State the blood parasite species.
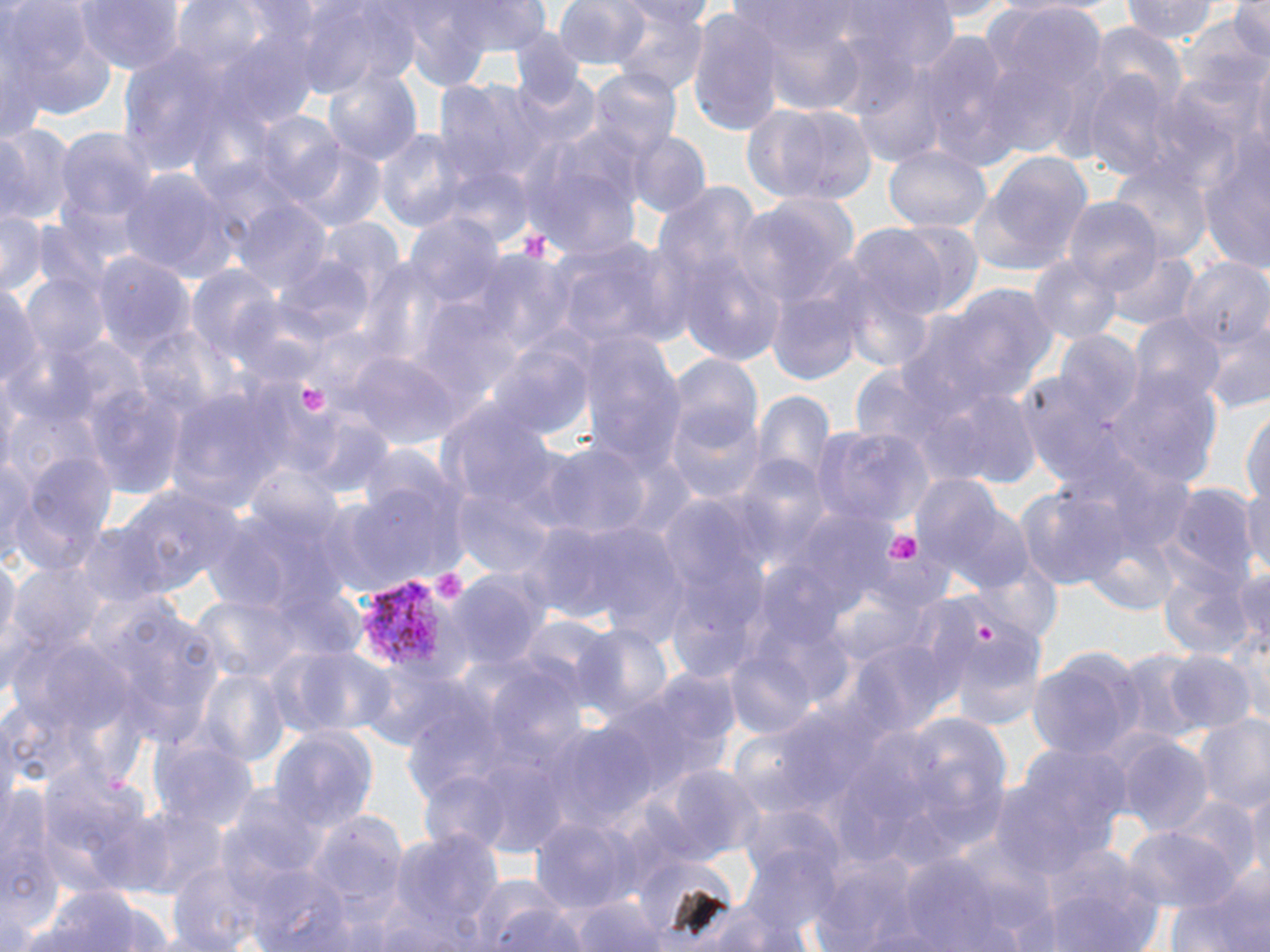
Plasmodium vivax.

Approximate bounding boxes as named x1/y1/x2/y2 corners in pixels. Uninfected red blood cell locations: (x1=74, y1=0, x2=185, y2=78), (x1=171, y1=0, x2=281, y2=83), (x1=295, y1=0, x2=422, y2=94), (x1=552, y1=0, x2=655, y2=69), (x1=1125, y1=0, x2=1222, y2=44), (x1=1230, y1=0, x2=1270, y2=64), (x1=439, y1=1, x2=553, y2=56), (x1=979, y1=1, x2=1106, y2=148), (x1=393, y1=2, x2=517, y2=85), (x1=4, y1=4, x2=119, y2=132), (x1=612, y1=7, x2=708, y2=98), (x1=687, y1=8, x2=785, y2=138), (x1=1086, y1=24, x2=1186, y2=113), (x1=909, y1=29, x2=1025, y2=167), (x1=107, y1=49, x2=230, y2=180), (x1=323, y1=66, x2=422, y2=169), (x1=589, y1=68, x2=680, y2=162), (x1=1080, y1=70, x2=1174, y2=178), (x1=434, y1=81, x2=550, y2=188), (x1=745, y1=101, x2=878, y2=204), (x1=249, y1=111, x2=347, y2=201), (x1=0, y1=123, x2=73, y2=230), (x1=55, y1=127, x2=155, y2=231), (x1=1198, y1=128, x2=1270, y2=274), (x1=626, y1=129, x2=710, y2=218), (x1=374, y1=130, x2=467, y2=235), (x1=520, y1=134, x2=643, y2=262), (x1=288, y1=140, x2=385, y2=232), (x1=881, y1=144, x2=993, y2=235), (x1=969, y1=153, x2=1093, y2=274), (x1=1109, y1=157, x2=1212, y2=266), (x1=441, y1=166, x2=533, y2=245), (x1=121, y1=172, x2=241, y2=285), (x1=652, y1=192, x2=792, y2=367), (x1=735, y1=196, x2=854, y2=312), (x1=1065, y1=199, x2=1164, y2=299), (x1=234, y1=200, x2=332, y2=294), (x1=1, y1=208, x2=44, y2=296), (x1=407, y1=214, x2=504, y2=311), (x1=883, y1=221, x2=983, y2=314), (x1=844, y1=227, x2=952, y2=330), (x1=554, y1=241, x2=672, y2=353), (x1=1106, y1=250, x2=1199, y2=334), (x1=89, y1=251, x2=195, y2=364), (x1=1030, y1=253, x2=1125, y2=346), (x1=279, y1=256, x2=373, y2=342), (x1=1183, y1=256, x2=1269, y2=352), (x1=185, y1=267, x2=281, y2=362), (x1=764, y1=272, x2=871, y2=387), (x1=0, y1=280, x2=44, y2=401), (x1=923, y1=282, x2=1060, y2=409), (x1=233, y1=299, x2=328, y2=389), (x1=1131, y1=313, x2=1226, y2=411), (x1=135, y1=325, x2=228, y2=422), (x1=1200, y1=325, x2=1270, y2=416), (x1=1054, y1=333, x2=1146, y2=424), (x1=580, y1=338, x2=687, y2=474), (x1=490, y1=341, x2=599, y2=444), (x1=348, y1=352, x2=464, y2=448), (x1=669, y1=359, x2=765, y2=460), (x1=1107, y1=370, x2=1222, y2=492), (x1=83, y1=382, x2=187, y2=500), (x1=916, y1=383, x2=1041, y2=489), (x1=751, y1=385, x2=836, y2=489), (x1=167, y1=386, x2=290, y2=512), (x1=664, y1=401, x2=767, y2=507), (x1=442, y1=402, x2=563, y2=516), (x1=1242, y1=406, x2=1270, y2=511), (x1=293, y1=410, x2=397, y2=500), (x1=813, y1=424, x2=932, y2=527), (x1=539, y1=442, x2=650, y2=542), (x1=0, y1=452, x2=37, y2=567), (x1=22, y1=452, x2=118, y2=555), (x1=341, y1=477, x2=466, y2=592), (x1=913, y1=480, x2=1035, y2=596), (x1=1243, y1=481, x2=1270, y2=582), (x1=1161, y1=482, x2=1260, y2=596), (x1=117, y1=483, x2=241, y2=596), (x1=451, y1=483, x2=561, y2=582), (x1=1012, y1=483, x2=1130, y2=594), (x1=545, y1=519, x2=689, y2=638), (x1=72, y1=523, x2=172, y2=611), (x1=0, y1=550, x2=20, y2=666), (x1=1232, y1=563, x2=1270, y2=662), (x1=1156, y1=566, x2=1261, y2=666), (x1=446, y1=568, x2=549, y2=672), (x1=944, y1=623, x2=1048, y2=731), (x1=576, y1=624, x2=673, y2=729), (x1=283, y1=643, x2=399, y2=739), (x1=724, y1=643, x2=820, y2=742), (x1=1026, y1=649, x2=1144, y2=759), (x1=1112, y1=650, x2=1208, y2=746), (x1=1162, y1=650, x2=1256, y2=734), (x1=616, y1=667, x2=742, y2=799), (x1=198, y1=669, x2=289, y2=767), (x1=485, y1=671, x2=587, y2=771), (x1=893, y1=712, x2=1012, y2=842), (x1=1192, y1=714, x2=1270, y2=814), (x1=543, y1=724, x2=655, y2=833), (x1=269, y1=728, x2=375, y2=833), (x1=149, y1=737, x2=257, y2=835), (x1=1118, y1=737, x2=1213, y2=837), (x1=987, y1=749, x2=1130, y2=879), (x1=654, y1=767, x2=764, y2=865), (x1=1239, y1=779, x2=1270, y2=882), (x1=227, y1=789, x2=330, y2=882), (x1=1169, y1=795, x2=1262, y2=883), (x1=118, y1=805, x2=228, y2=897), (x1=304, y1=809, x2=412, y2=924), (x1=530, y1=817, x2=635, y2=915), (x1=1121, y1=828, x2=1239, y2=917), (x1=392, y1=829, x2=506, y2=943), (x1=942, y1=844, x2=1063, y2=949), (x1=165, y1=847, x2=291, y2=952), (x1=809, y1=847, x2=926, y2=950), (x1=899, y1=851, x2=1002, y2=950), (x1=1036, y1=854, x2=1164, y2=952), (x1=241, y1=861, x2=360, y2=951), (x1=1164, y1=870, x2=1269, y2=951), (x1=467, y1=873, x2=582, y2=952), (x1=26, y1=882, x2=155, y2=952), (x1=573, y1=895, x2=671, y2=952), (x1=672, y1=902, x2=802, y2=952). Plasmodium vivax-infected red blood cell locations: (x1=356, y1=578, x2=471, y2=688). Platelet locations: (x1=517, y1=232, x2=550, y2=262), (x1=299, y1=385, x2=329, y2=410), (x1=883, y1=529, x2=922, y2=562), (x1=429, y1=566, x2=468, y2=608), (x1=975, y1=617, x2=1000, y2=648). Image is 1270×952 pixels. Light microscopy. May-Grünwald-Giemsa stain. One field of a larger specimen. Captured at 1000x magnification. Thin blood film.